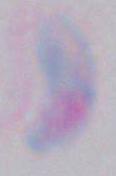

{
  "modality": "micrograph",
  "magnification": "1000x",
  "identification": "Toxoplasma gondii"
}